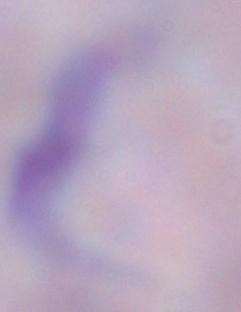

A trypanosome is shown. 1000x magnification. Photomicrograph.